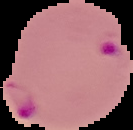
Cell region segmented out of the field of view; the surrounding area is masked to black. Image is 133×130 pixels. From a thin blood smear. Malaria status: parasitized.